Locate every malaria parasite.
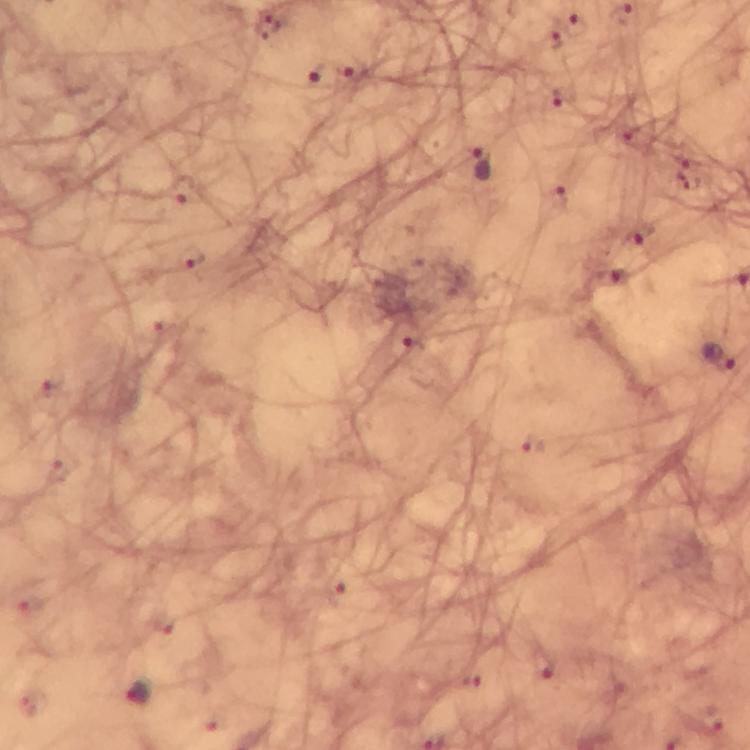

Approximate centers as (x, y) in pixels.
Malaria parasites: (576, 25), (557, 38), (349, 65), (320, 74), (566, 96), (482, 162), (181, 190), (554, 198), (637, 235), (190, 257), (414, 351), (722, 359), (532, 445), (336, 592), (541, 668), (139, 694), (711, 721).

Summary:
  - Capture: smartphone photograph through a microscope
  - Immersion oil: applied
  - Stain: Giemsa
  - Magnification: 100x
  - Preparation: thick smear
  - Cropped from: one field of view
  - Context: from a malaria diagnostic workup
  - Image size: 750×750 pixels